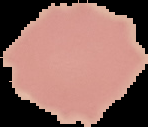

From a thin blood smear. Malaria status: uninfected. Image is 148×127 pixels. Segmented cell region on a black background.